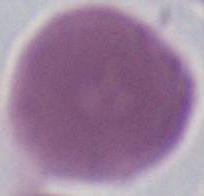 Captured at 1000x magnification. Photomicrograph. A red blood cell is seen.